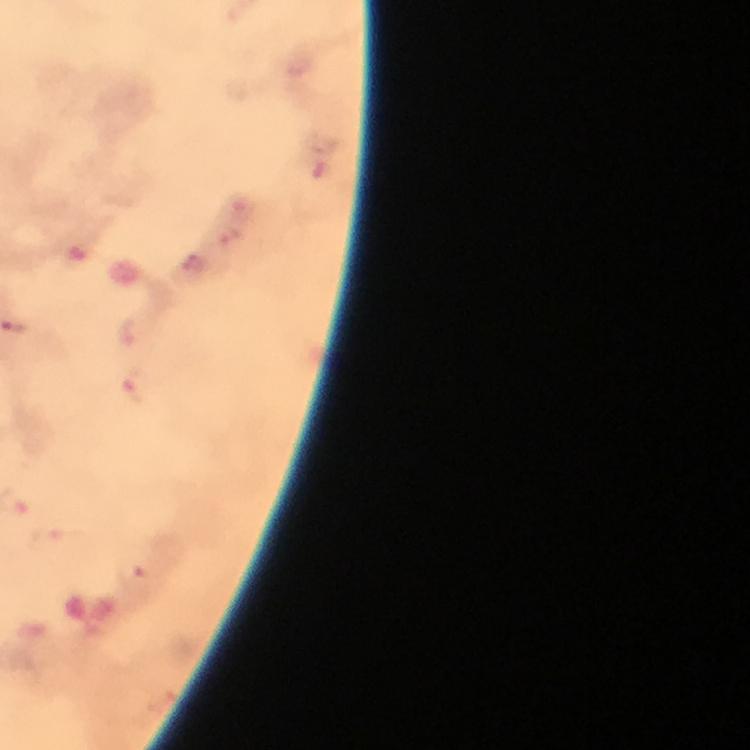
capture = smartphone camera through the microscope
immersion oil = used
stain = Giemsa
cropped from = one field of view
malaria parasite locations = approximate centers as (x, y) in pixels: (127, 331), (135, 385), (130, 572)
magnification = 100x
context = from a malaria diagnostic workup
image size = 750×750 pixels
preparation = thick blood film